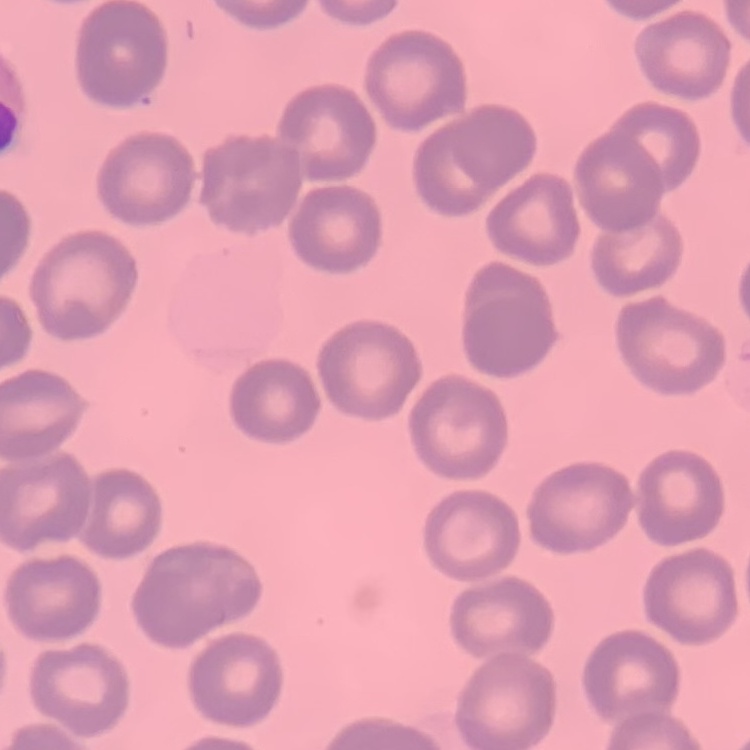
The erythrocytes exhibit no rouleaux formation. One tile cut from a larger photomicrograph. Stained with either Field's or Giemsa. Thin peripheral smear.